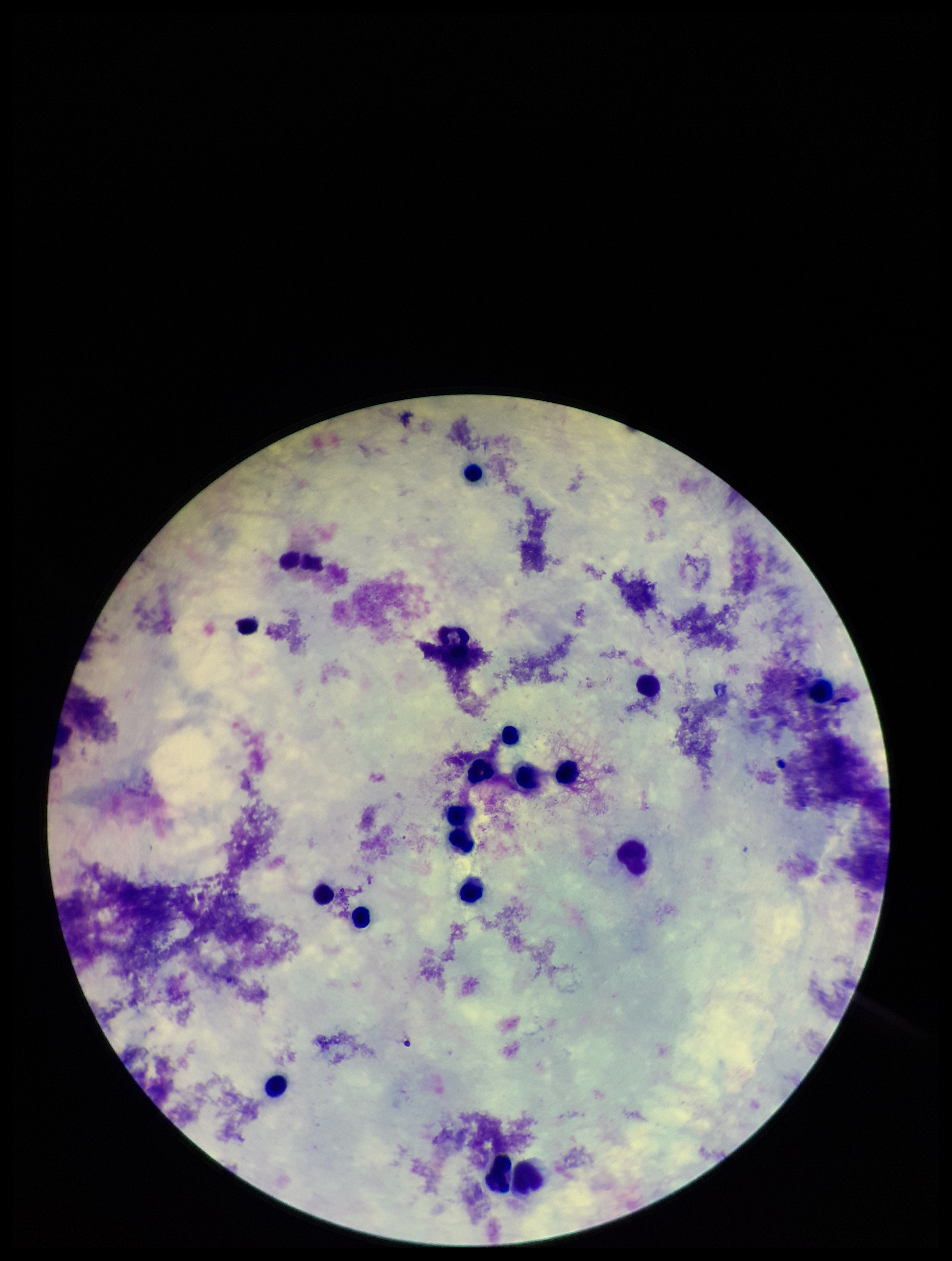 Patient malaria status: negative. Photographed through the microscope eyepiece with a smartphone camera. Preparation: thick blood smear. Parasite count: 0. Plasmodium parasites: none detected. Stained with Giemsa. One field from this slide. Leukocyte count: 19. Image is 952×1261 pixels.